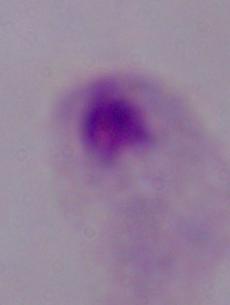

magnification = 1000x
modality = photomicrograph
identification = trichomonad